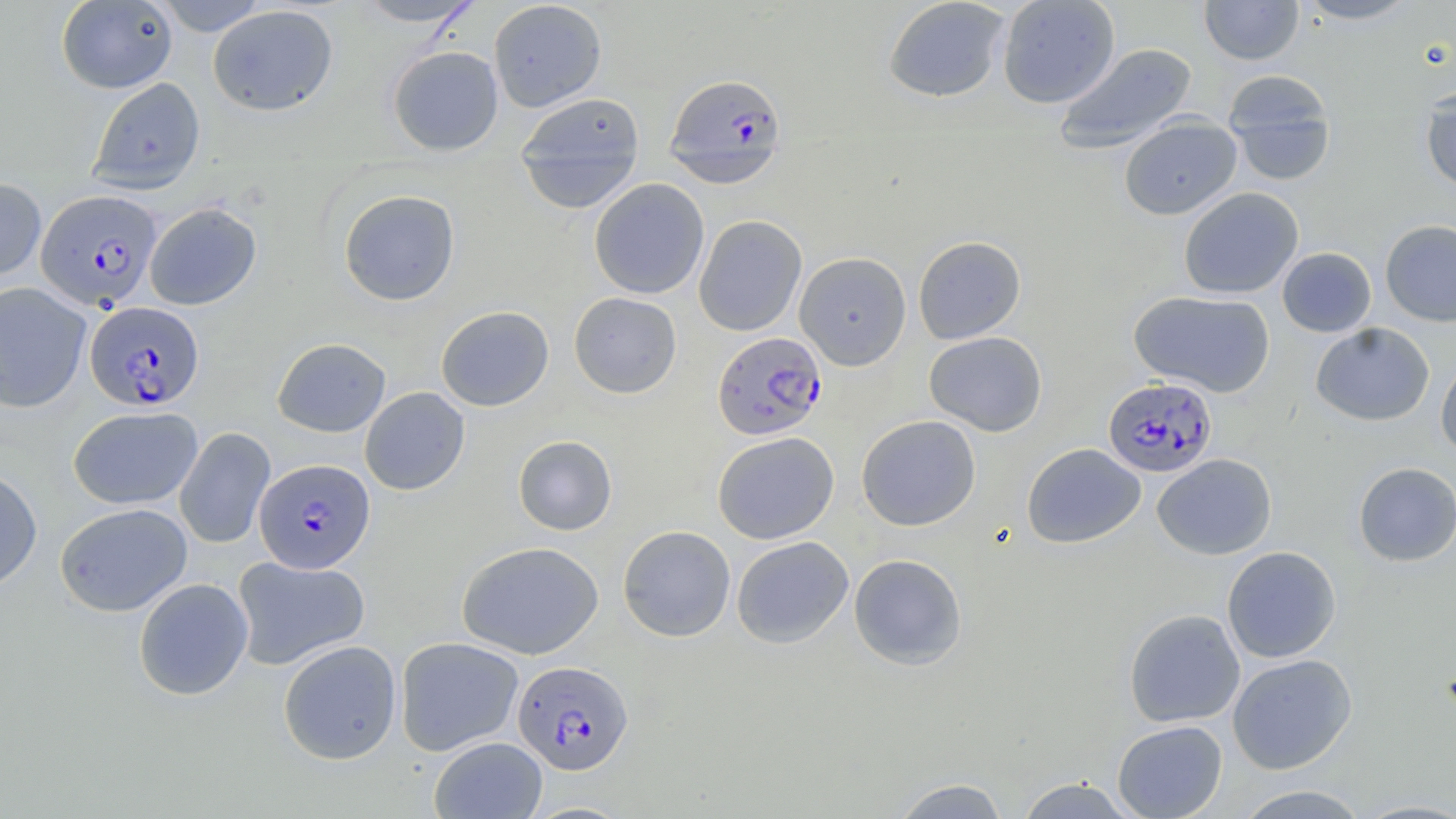
Summary:
  - Coordinate format: approximate bounding boxes as (x1, y1, x2, y2) in pixels
  - Uninfected red blood cell locations: (56, 0, 178, 94), (151, 0, 270, 36), (352, 0, 484, 28), (488, 0, 607, 112), (882, 0, 1010, 103), (996, 0, 1120, 108), (1199, 0, 1304, 65), (1295, 0, 1419, 24), (208, 5, 338, 116), (1053, 42, 1198, 154), (387, 46, 504, 155), (1224, 71, 1337, 185), (88, 77, 205, 195), (1420, 87, 1456, 194), (513, 92, 646, 211), (1118, 115, 1242, 220), (0, 178, 46, 281), (589, 178, 709, 299), (1178, 187, 1303, 299), (338, 189, 460, 306), (144, 202, 262, 310), (693, 215, 807, 336), (1379, 220, 1456, 327), (913, 235, 1026, 343), (1277, 247, 1377, 337), (794, 251, 911, 369), (0, 282, 91, 413), (1129, 290, 1275, 398), (569, 292, 682, 398), (436, 306, 554, 411), (1310, 322, 1435, 426), (924, 331, 1047, 436), (272, 337, 391, 437), (1436, 353, 1456, 462), (360, 387, 470, 495), (68, 406, 202, 509), (856, 415, 981, 531), (174, 427, 276, 549), (712, 431, 839, 544), (513, 435, 617, 535), (1022, 443, 1146, 549), (1152, 454, 1277, 560), (1353, 461, 1456, 566), (0, 467, 42, 593), (55, 503, 192, 616), (617, 525, 736, 642), (731, 536, 854, 649), (457, 541, 604, 659), (1222, 546, 1341, 663), (848, 553, 968, 670), (231, 555, 370, 670), (133, 577, 253, 701), (1123, 609, 1245, 727), (395, 636, 523, 756), (278, 640, 402, 764), (1227, 653, 1357, 774), (1112, 720, 1228, 819), (429, 736, 547, 818), (1014, 776, 1138, 818), (890, 777, 1011, 819), (1231, 785, 1370, 818)
  - Plasmodium falciparum-infected red blood cell locations: (664, 73, 788, 186), (35, 189, 162, 311), (85, 301, 204, 412), (712, 331, 827, 440), (1103, 377, 1217, 479), (254, 458, 376, 573), (512, 659, 634, 775)
  - Slide-level diagnosis: Plasmodium falciparum
  - Preparation: thin blood smear
  - Modality: light microscopy
  - Image size: 1456×819 pixels
  - Stain: May-Grünwald-Giemsa
  - Magnification: 1000x
  - Field of view: single